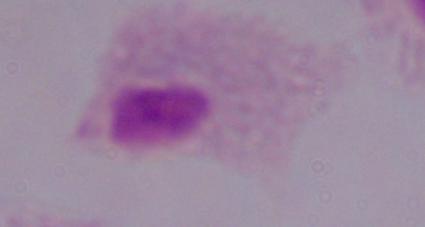
{
  "magnification": "1000x",
  "modality": "photomicrograph",
  "identification": "trichomonad"
}